Assess this cell for malaria.
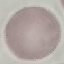
Uninfected.

{
  "capture": "smartphone camera at the microscope eyepiece",
  "stain": "Giemsa",
  "preparation": "thin smear",
  "image_type": "automatically extracted cell patch, resized to 64 × 64 pixels"
}